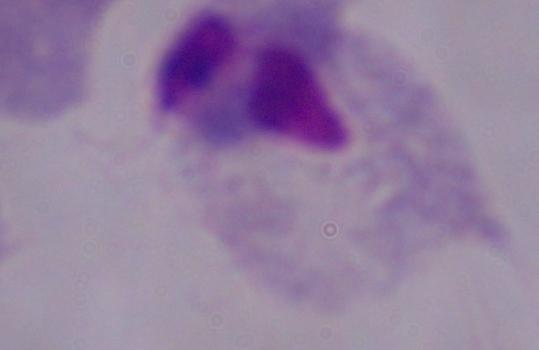

Summary:
  - Identification: trichomonad
  - Modality: photomicrograph
  - Magnification: 1000x